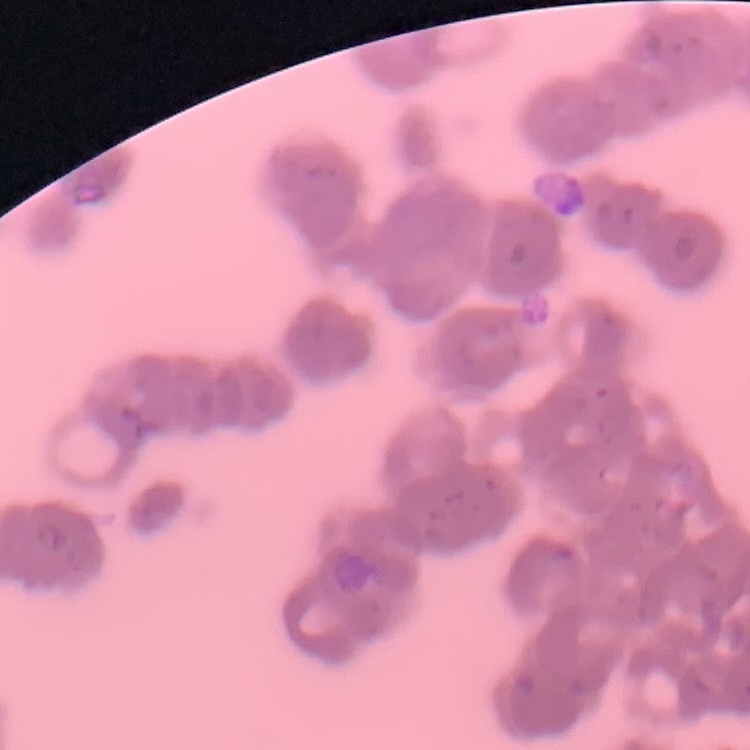
Summary:
  - Erythrocyte morphology: rouleaux formation
  - Preparation: thin blood film
  - Image type: one tile cut from a larger photomicrograph
  - Stain: Field's or Giemsa